State the preparation type.
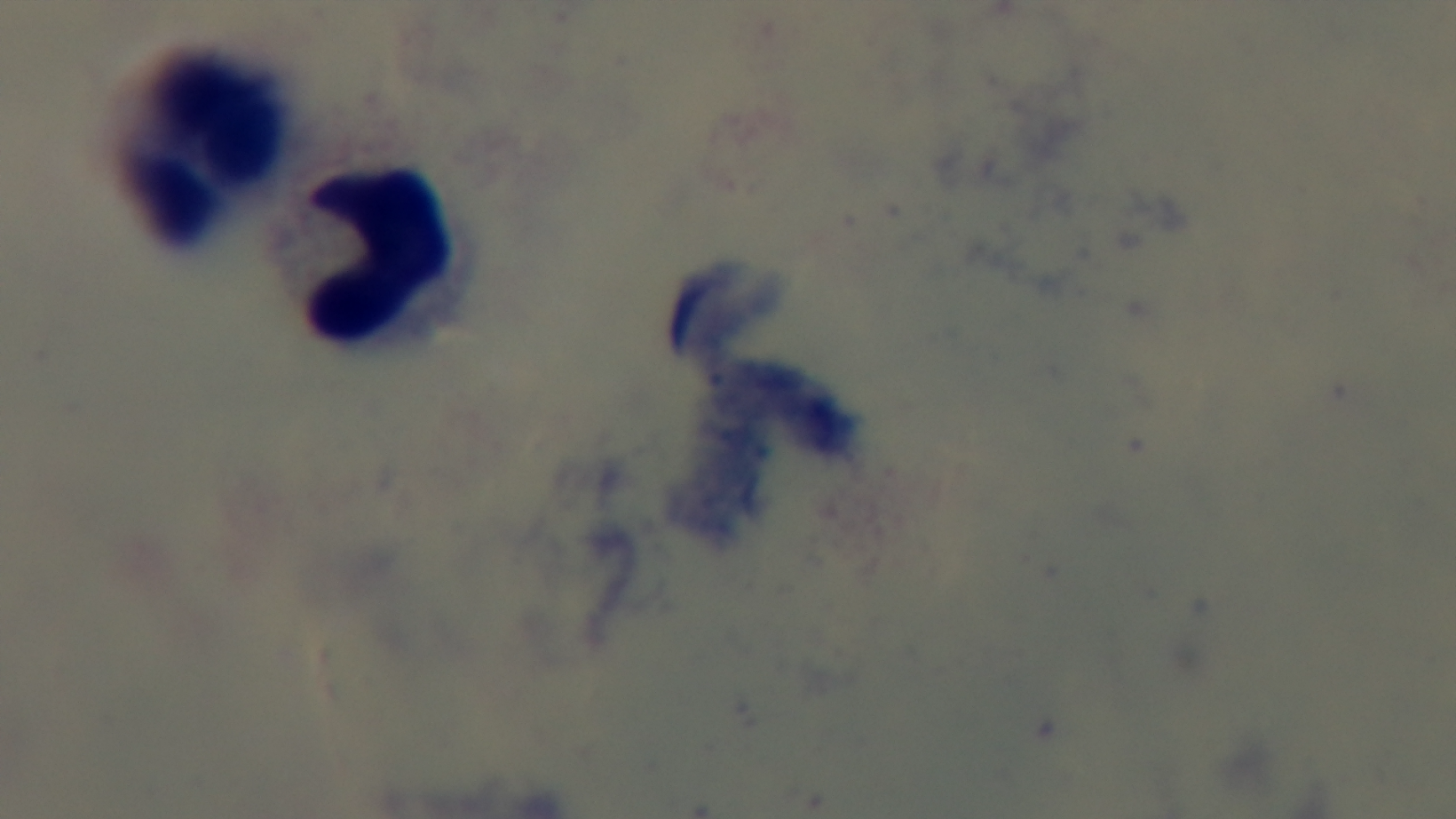

It is a thick blood film.

{
  "malaria_status": "uninfected",
  "objective": "100x oil immersion",
  "modality": "light microscopy",
  "capture": "mounted 4K digital camera",
  "stain": "Giemsa",
  "field_of_view": "single"
}